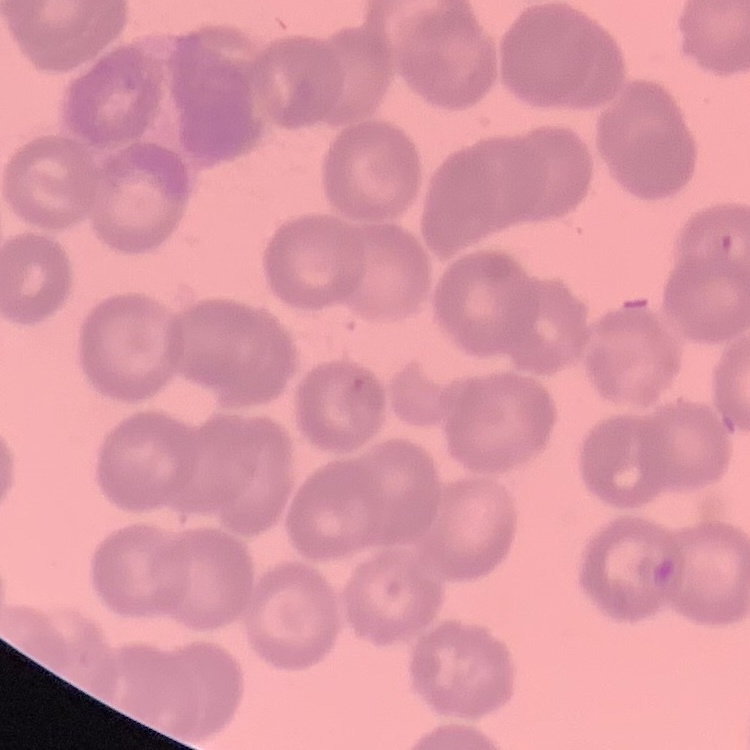

Summary:
  - Erythrocyte morphology: rouleaux formation
  - Preparation: thin peripheral smear
  - Image type: square crop of a larger photomicrograph
  - Stain: Field's or Giemsa